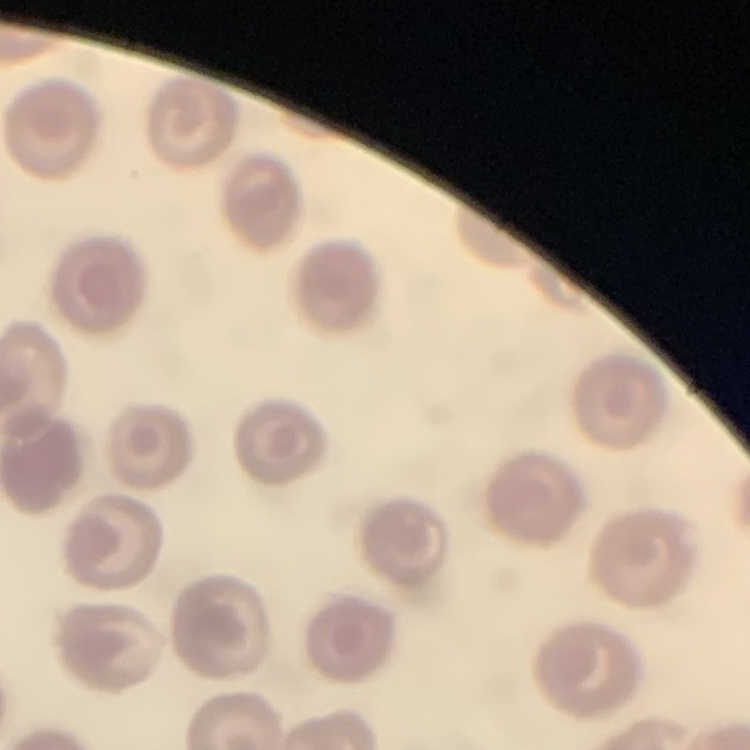 The erythrocytes exhibit no rouleaux formation. Stained with either Field's or Giemsa. Thin peripheral smear. Square crop of a larger photomicrograph.